Outline each blood parasite and name the species.
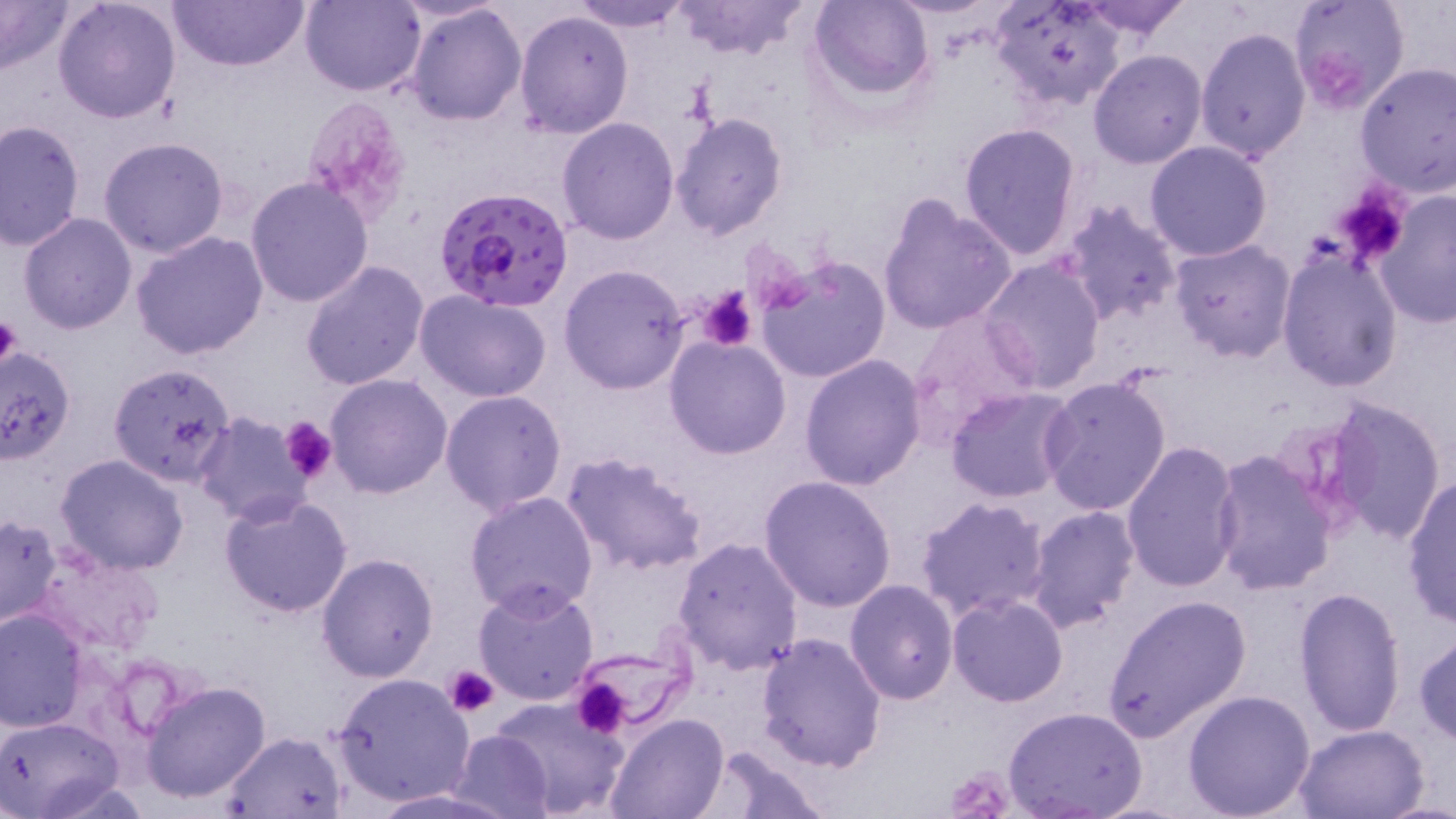
Approximate bounding boxes as (x1, y1, x2, y2) in pixels.
Plasmodium falciparum-infected red blood cells: (436, 186, 573, 313).
No Plasmodium ovale, Plasmodium malariae, Plasmodium vivax, Babesia divergens, or Trypanosoma brucei observed.

Uninfected red blood cell locations: (52, 0, 182, 122), (167, 0, 310, 72), (300, 0, 423, 97), (570, 0, 690, 33), (669, 0, 810, 62), (809, 0, 934, 101), (988, 0, 1126, 111), (1076, 0, 1193, 40), (1287, 0, 1412, 115), (0, 1, 75, 75), (407, 4, 526, 126), (514, 10, 634, 138), (1195, 27, 1309, 162), (1089, 49, 1208, 168), (1356, 63, 1456, 196), (669, 110, 789, 239), (556, 117, 679, 244), (1, 119, 86, 251), (958, 121, 1083, 259), (99, 136, 231, 258), (1144, 141, 1274, 262), (245, 175, 375, 307), (1375, 192, 1456, 328), (878, 193, 1017, 336), (1057, 200, 1183, 328), (17, 212, 138, 333), (130, 231, 269, 360), (1168, 239, 1296, 365), (1277, 249, 1404, 394), (755, 255, 891, 384), (980, 259, 1107, 393), (300, 260, 431, 392), (559, 263, 692, 395), (415, 291, 552, 403), (903, 308, 1044, 449), (664, 335, 791, 460), (0, 345, 77, 468), (798, 355, 926, 490), (107, 362, 236, 485), (324, 373, 452, 499), (1038, 375, 1171, 517), (944, 387, 1076, 502), (440, 390, 568, 517), (1322, 395, 1449, 545), (194, 412, 316, 527), (1120, 440, 1242, 593), (1208, 450, 1339, 597), (560, 452, 709, 578), (53, 453, 190, 575), (758, 475, 898, 613), (1401, 476, 1456, 627), (464, 490, 599, 617), (219, 492, 353, 618), (914, 496, 1054, 626), (1025, 505, 1141, 633), (1, 514, 63, 630), (672, 535, 804, 675), (29, 545, 165, 658), (316, 552, 438, 683), (472, 579, 600, 704), (845, 579, 959, 703), (1292, 587, 1408, 737), (948, 593, 1069, 707), (1101, 594, 1253, 742), (0, 609, 87, 734), (1413, 631, 1456, 744), (756, 632, 888, 772), (567, 642, 690, 734), (330, 674, 473, 808), (141, 680, 271, 803), (1181, 688, 1316, 817), (483, 696, 633, 819), (1004, 708, 1148, 819), (605, 712, 730, 819), (0, 715, 124, 819), (1292, 724, 1431, 818), (220, 730, 349, 817), (448, 730, 553, 819), (698, 743, 830, 817), (366, 788, 526, 817). Platelet locations: (1314, 52, 1365, 106), (303, 96, 410, 219), (1341, 200, 1400, 259), (698, 287, 758, 351), (0, 313, 23, 374), (279, 416, 338, 486), (443, 665, 500, 718), (571, 676, 633, 739), (944, 761, 1016, 819). Slide-level diagnosis: Plasmodium falciparum. Image is 1456×819 pixels. Thin blood smear. May-Grünwald-Giemsa stain. Light microscopy. Captured at 1000x magnification. Single field of view.